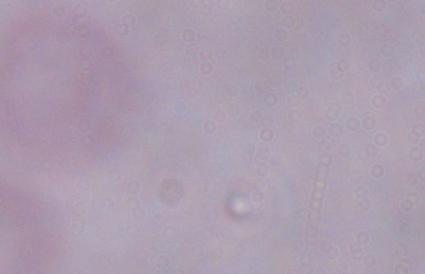
Captured at 1000x magnification. Micrograph. A trypanosome is shown.